Identify the cell.
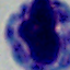
A leukocyte.

modality = micrograph
magnification = 1000x